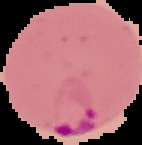
malaria status = parasitized
preparation = thin blood film
image size = 142×145 pixels
image type = segmented cell region with the area outside set to black